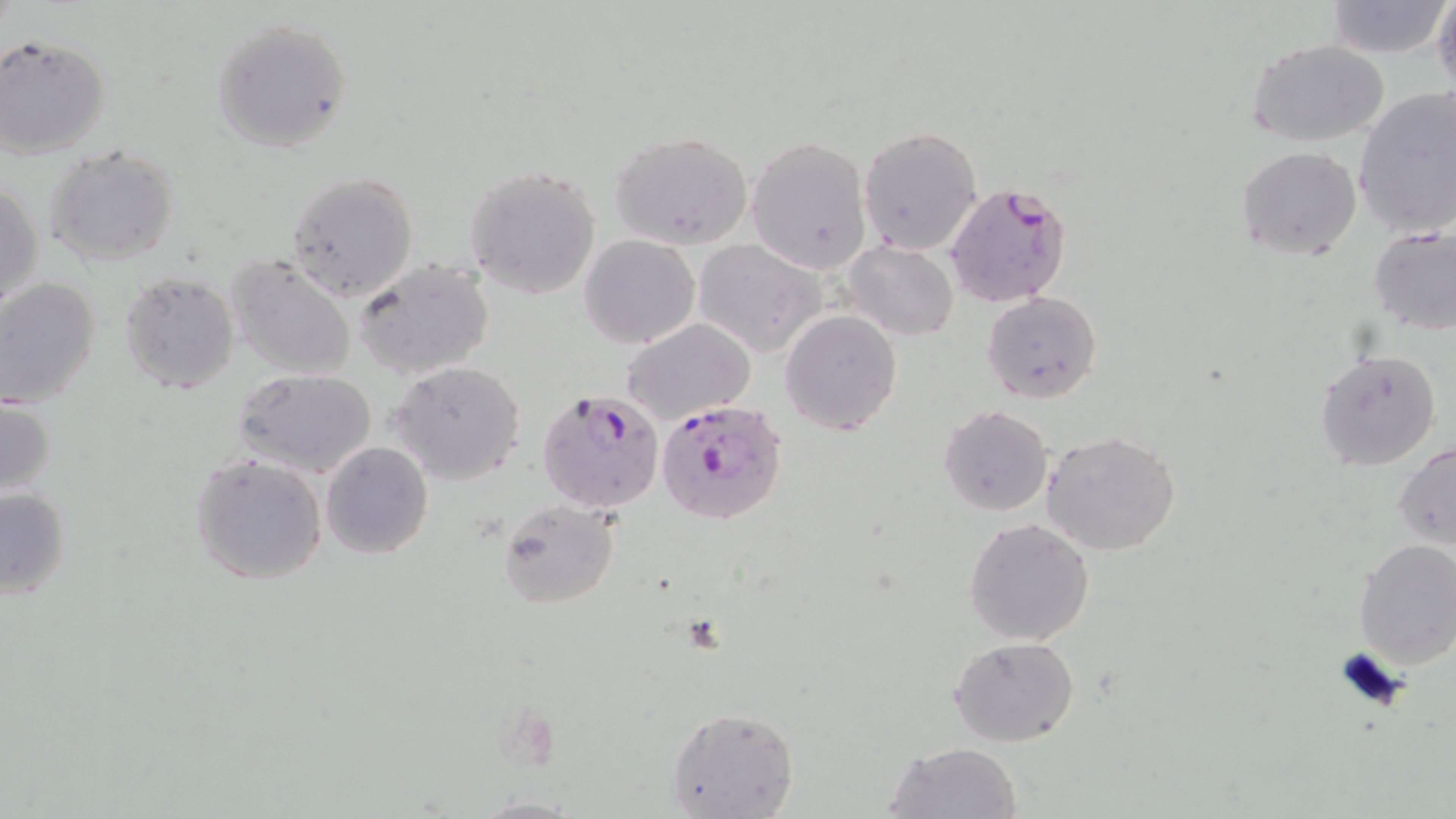 Approximate bounding boxes as (x1,y1)-(x2,y2) corner pairs in pixels. Plasmodium falciparum-infected red blood cell locations: (945,182)-(1070,309), (538,389)-(666,511), (655,398)-(788,525). Uninfected red blood cell locations: (1433,0)-(1456,95), (1324,2)-(1449,58), (210,17)-(353,154), (0,32)-(112,159), (1248,39)-(1391,147), (1353,87)-(1456,239), (858,125)-(984,255), (609,131)-(755,249), (747,136)-(872,273), (44,144)-(182,267), (1236,145)-(1363,263), (464,166)-(601,300), (286,172)-(418,302), (1,182)-(43,315), (1368,224)-(1456,335), (580,234)-(700,349), (692,238)-(826,359), (844,242)-(958,341), (227,255)-(358,382), (354,258)-(493,381), (118,269)-(241,394), (0,277)-(101,408), (982,292)-(1102,405), (780,309)-(903,435), (620,318)-(755,427), (1312,349)-(1442,471), (389,360)-(528,486), (235,369)-(377,477), (0,396)-(56,501), (938,405)-(1053,515), (1044,431)-(1182,556), (320,440)-(433,559), (1395,441)-(1456,550), (189,452)-(327,585), (0,485)-(72,600), (496,499)-(621,609), (964,518)-(1094,645), (1352,537)-(1456,670), (949,637)-(1078,747), (666,704)-(799,819), (882,740)-(1023,819). Slide-level diagnosis: Plasmodium falciparum. Captured at 1000x magnification. Thin blood film. Light microscopy. May-Grünwald-Giemsa stain. Single field of view. Image is 1456×819 pixels.